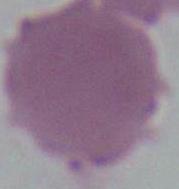 Photomicrograph. An erythrocyte is seen. Captured at 1000x magnification.